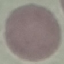

Summary:
  - Malaria status: uninfected
  - Preparation: thin smear
  - Stain: Giemsa
  - Capture: smartphone camera at the microscope eyepiece
  - Image type: cell patch, automatically extracted from a larger field of view and resized to 64 × 64 pixels